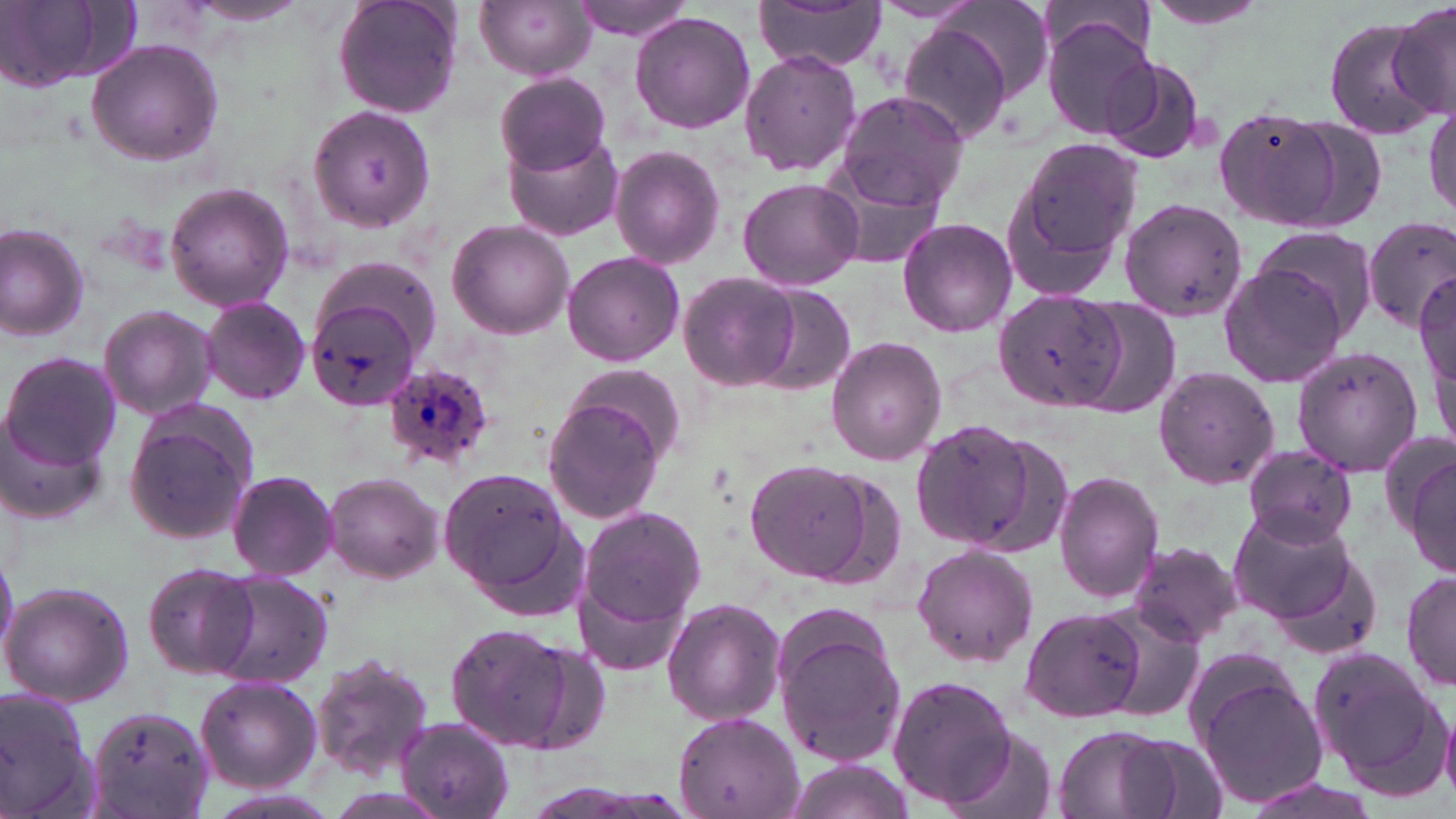
Approximate bounding boxes as (x1,y1)-(x2,y2) corner pairs in pixels. Plasmodium ovale-infected red blood cell locations: (381,362)-(499,472). Uninfected red blood cell locations: (332,0)-(465,120), (475,0)-(595,79), (572,0)-(698,41), (753,0)-(887,72), (1140,0)-(1281,32), (932,1)-(1057,107), (1,2)-(123,90), (1386,2)-(1456,126), (630,11)-(757,134), (1040,13)-(1162,141), (1321,15)-(1443,141), (897,22)-(1014,143), (84,38)-(225,168), (738,48)-(861,177), (1098,53)-(1209,164), (492,73)-(613,176), (832,90)-(970,208), (1424,95)-(1456,224), (310,105)-(436,232), (1211,105)-(1345,232), (1262,110)-(1391,236), (505,132)-(624,241), (1006,135)-(1141,293), (611,146)-(727,268), (738,178)-(863,290), (166,183)-(295,311), (1119,199)-(1248,322), (897,216)-(1018,337), (446,218)-(576,340), (1361,218)-(1456,328), (0,222)-(92,342), (1251,225)-(1379,339), (562,252)-(686,366), (1219,261)-(1349,391), (678,270)-(803,391), (1416,270)-(1454,417), (754,285)-(857,397), (994,291)-(1124,410), (199,296)-(312,406), (306,296)-(421,409), (1064,296)-(1183,421), (98,304)-(217,422), (826,335)-(947,465), (1290,345)-(1424,476), (4,351)-(120,472), (562,366)-(689,469), (1152,366)-(1279,490), (542,391)-(670,526), (0,400)-(105,528), (123,402)-(258,547), (912,419)-(1043,551), (1244,446)-(1357,548), (1403,447)-(1455,578), (745,460)-(874,582), (438,465)-(581,603), (226,470)-(340,580), (323,471)-(444,582), (1054,471)-(1164,604), (1228,504)-(1359,624), (580,506)-(709,636), (1127,541)-(1246,648), (911,543)-(1037,667), (142,563)-(260,679), (1401,570)-(1456,691), (210,571)-(334,687), (2,581)-(134,706), (661,597)-(786,725), (1092,601)-(1207,725), (1025,605)-(1145,717), (771,610)-(909,771), (445,623)-(572,751), (517,637)-(611,753), (1311,646)-(1448,784), (311,653)-(435,778), (887,674)-(1019,809), (195,676)-(321,792), (1197,676)-(1330,809), (0,686)-(103,819), (1439,700)-(1456,800), (85,705)-(214,819), (671,714)-(803,819), (395,716)-(516,818), (1051,725)-(1179,819), (941,727)-(1059,819), (1119,733)-(1230,819), (781,758)-(916,819), (1236,776)-(1384,819). Slide-level diagnosis: Plasmodium ovale. Light microscopy. Single field of view. May-Grünwald-Giemsa stain. Image is 1456×819 pixels. Captured at 1000x magnification. Thin blood smear.